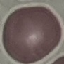

Result: negative for malaria parasites. Thin blood film. Giemsa stain. Automatically extracted cell patch, resized to 64 × 64 pixels. Acquired by smartphone through the microscope eyepiece.